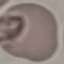

malaria status = uninfected
image type = automatically extracted cell patch, resized to 64 × 64 pixels
capture = smartphone camera at the microscope eyepiece
stain = Giemsa
preparation = thin smear